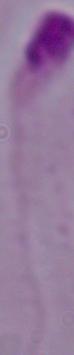

Summary:
  - Magnification: 1000x
  - Modality: micrograph
  - Identification: Leishmania